State the blood parasite species.
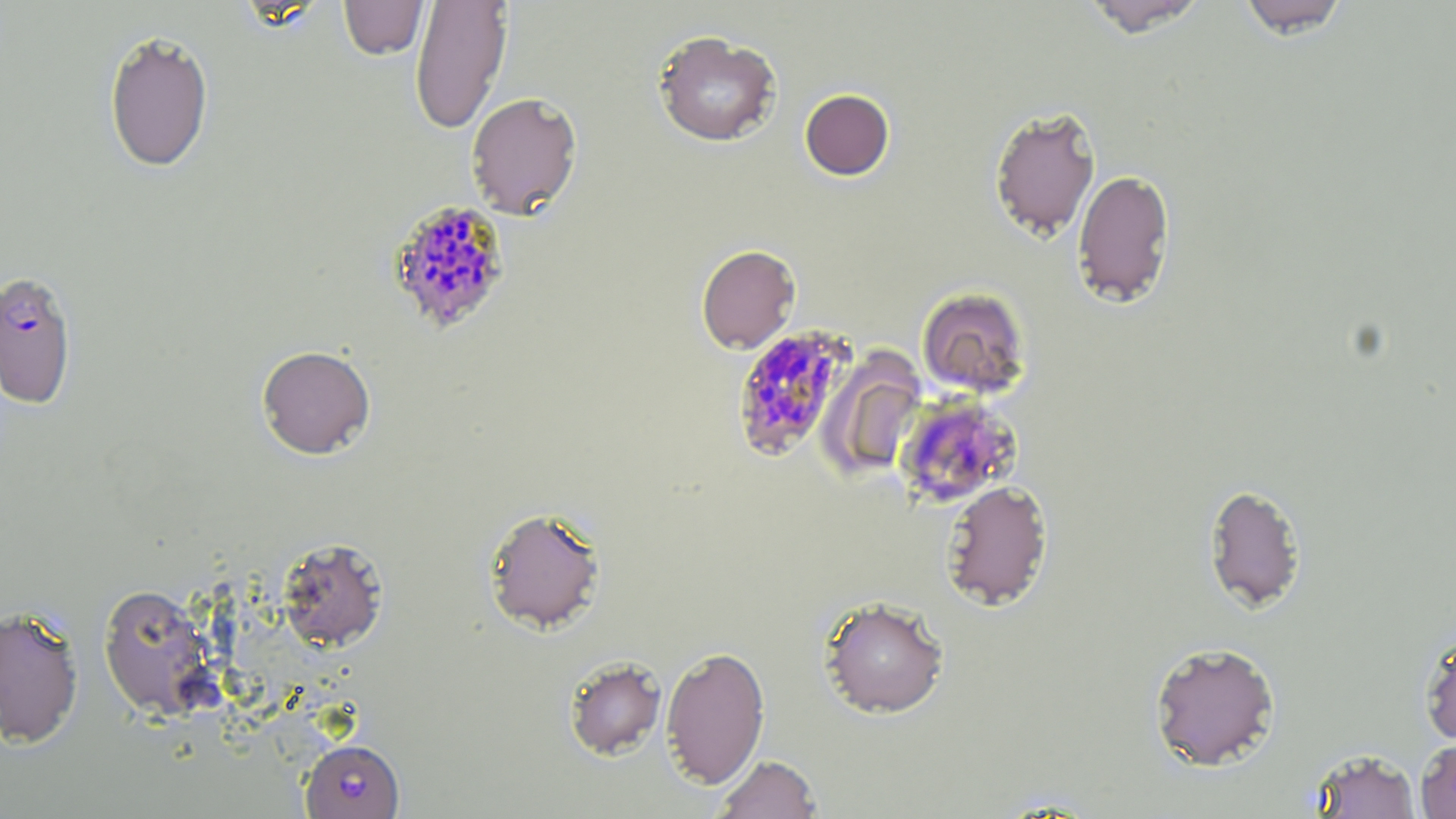

Plasmodium falciparum.

Approximate bounding boxes as named x1/y1/x2/y2 corners in pixels. Uninfected red blood cell locations: (x1=339, y1=0, x2=429, y2=60), (x1=409, y1=0, x2=513, y2=134), (x1=1080, y1=0, x2=1211, y2=37), (x1=1236, y1=0, x2=1352, y2=37), (x1=103, y1=29, x2=215, y2=172), (x1=652, y1=29, x2=782, y2=147), (x1=799, y1=88, x2=895, y2=180), (x1=465, y1=92, x2=583, y2=218), (x1=988, y1=106, x2=1101, y2=242), (x1=1072, y1=169, x2=1176, y2=308), (x1=696, y1=244, x2=801, y2=353), (x1=916, y1=286, x2=1031, y2=398), (x1=256, y1=345, x2=376, y2=459), (x1=820, y1=351, x2=927, y2=481), (x1=940, y1=479, x2=1053, y2=611), (x1=1203, y1=482, x2=1307, y2=612), (x1=483, y1=506, x2=607, y2=635), (x1=275, y1=537, x2=389, y2=653), (x1=97, y1=583, x2=220, y2=721), (x1=818, y1=595, x2=950, y2=718), (x1=0, y1=605, x2=85, y2=749), (x1=1418, y1=625, x2=1456, y2=747), (x1=1148, y1=640, x2=1281, y2=771), (x1=660, y1=645, x2=770, y2=789), (x1=563, y1=655, x2=667, y2=760), (x1=1415, y1=737, x2=1456, y2=818), (x1=1309, y1=747, x2=1422, y2=819), (x1=713, y1=754, x2=822, y2=818). Plasmodium falciparum-infected red blood cell locations: (x1=386, y1=199, x2=512, y2=335), (x1=0, y1=271, x2=78, y2=409), (x1=730, y1=325, x2=856, y2=461), (x1=895, y1=395, x2=1021, y2=507), (x1=301, y1=738, x2=404, y2=818). Light microscopy. Image is 1456×819 pixels. May-Grünwald-Giemsa stain. 1000x magnification. Thin blood film. Single field of view.